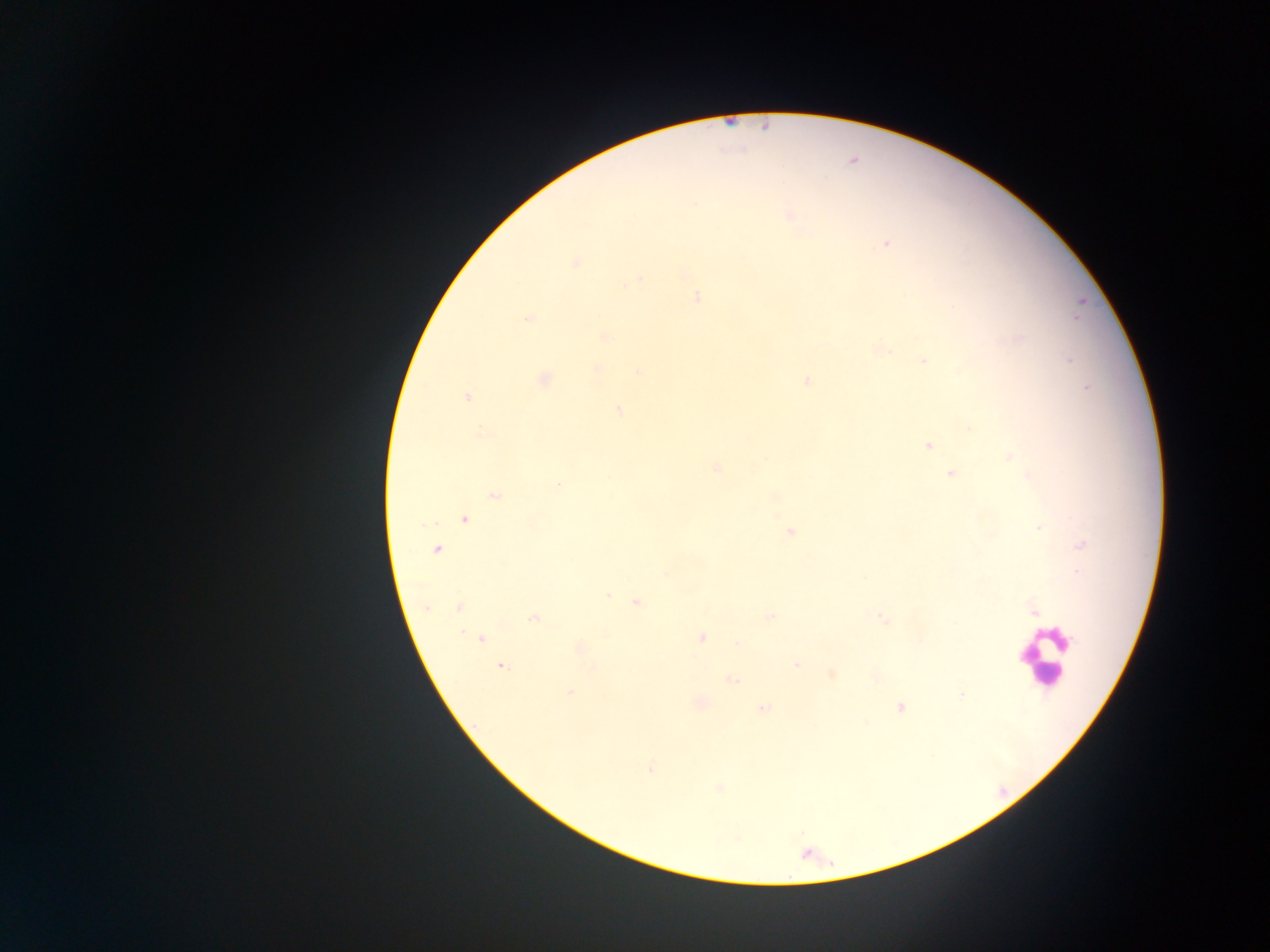
capture: mobile-phone photograph through a microscope
image_size: 1270×952 pixels
leukocyte_locations: 'approximate centers as [x, y] in pixels: [1045, 656]'
country: Ghana
field_of_view: single
preparation: thick blood smear
plasmodium_parasite_locations: 'approximate centers as [x, y] in pixels: [789, 216], [886, 244], [575, 262], [638, 279], [697, 297], [1076, 317], [528, 319], [605, 336], [1070, 359], [922, 360], [598, 368], [639, 373], [544, 379], [806, 382], [1086, 388], [468, 397], [619, 410], [969, 429], [482, 433], [929, 446], [1010, 456], [716, 468], [950, 473], [557, 485], [495, 495], [464, 519], [1038, 527], [790, 532], [1081, 545], [437, 550], [1078, 572], [666, 573], [608, 595], [637, 603], [458, 607], [427, 608], [1033, 611], [769, 617], [534, 618], [882, 619], [481, 637], [701, 637], [737, 643], [580, 649], [796, 665], [502, 666], [832, 674], [732, 680], [570, 692], [962, 695], [901, 707], [763, 709], [650, 769], [719, 787]'